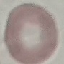

result = no malaria parasites detected
preparation = thin smear
capture = smartphone camera at the microscope eyepiece
stain = Giemsa
image type = automatically extracted cell patch, resized to 64 × 64 pixels